Give the extent of all Plasmodium falciparum-infected red blood cells.
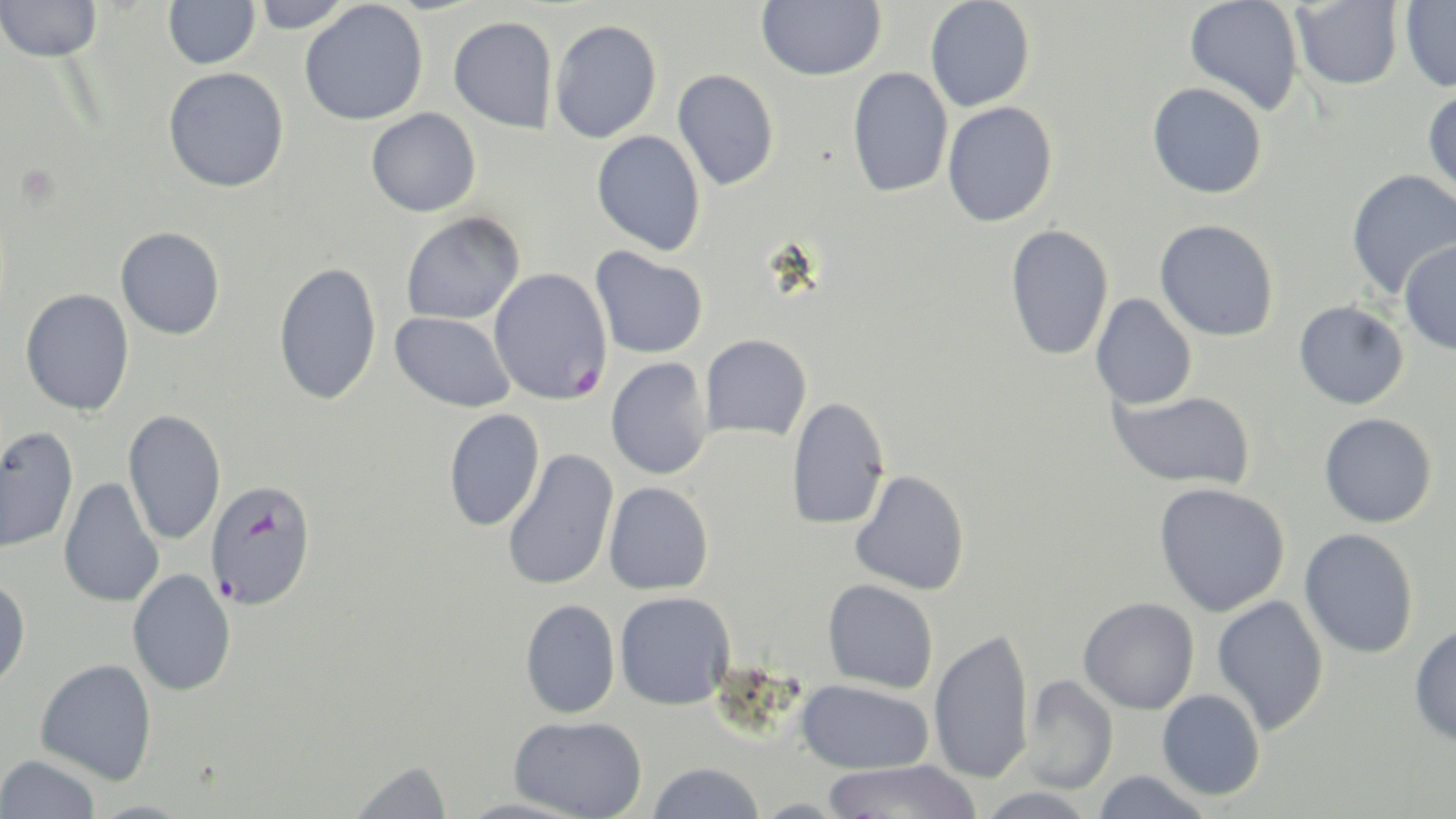
Approximate bounding boxes as (x1,y1)-(x2,y2) corner pairs in pixels.
Plasmodium falciparum-infected red blood cells: (489,267)-(613,405), (204,478)-(317,611).

Uninfected red blood cell locations: (0,0)-(102,63), (163,0)-(260,69), (250,0)-(356,33), (756,0)-(886,81), (924,0)-(1035,113), (1184,0)-(1304,115), (1291,1)-(1404,92), (1399,1)-(1456,92), (299,2)-(428,126), (448,15)-(558,133), (549,19)-(662,143), (162,67)-(289,193), (847,67)-(953,198), (672,69)-(780,191), (1147,82)-(1267,199), (1422,87)-(1456,202), (942,101)-(1059,227), (366,108)-(481,217), (591,130)-(706,256), (1345,168)-(1456,299), (400,212)-(525,326), (1154,219)-(1279,342), (1004,224)-(1114,362), (115,226)-(226,340), (1398,241)-(1456,356), (589,246)-(708,359), (273,261)-(383,407), (20,288)-(135,416), (1090,293)-(1197,410), (1293,300)-(1409,410), (389,312)-(516,412), (700,334)-(811,440), (605,357)-(714,480), (1108,389)-(1255,490), (786,397)-(890,530), (443,408)-(545,532), (123,409)-(227,545), (1319,413)-(1437,529), (0,426)-(79,556), (501,449)-(619,592), (850,469)-(970,596), (58,476)-(165,608), (603,482)-(714,595), (1153,482)-(1290,618), (1299,528)-(1418,658), (127,568)-(237,697), (0,576)-(31,690), (822,579)-(939,694), (614,591)-(735,710), (1211,594)-(1329,735), (1078,597)-(1199,714), (519,598)-(621,719), (1409,622)-(1456,749), (929,628)-(1035,785), (35,658)-(158,785), (1021,674)-(1120,795), (796,679)-(933,775), (1157,689)-(1266,800), (509,715)-(647,818), (1,754)-(101,818), (346,759)-(454,819), (825,760)-(978,819), (647,762)-(765,819), (1092,770)-(1212,819), (978,787)-(1098,819). Slide-level diagnosis: Plasmodium falciparum. May-Grünwald-Giemsa stain. Light microscopy. Thin blood smear. 1000x magnification. One field of a larger specimen. Image is 1456×819 pixels.